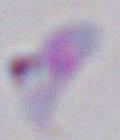

{
  "magnification": "1000x",
  "identification": "Toxoplasma gondii",
  "modality": "micrograph"
}